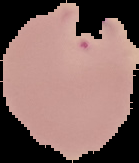

Segmented cell region on a black background. From a thin blood film. Image is 139×163 pixels. Malaria status: parasitized.